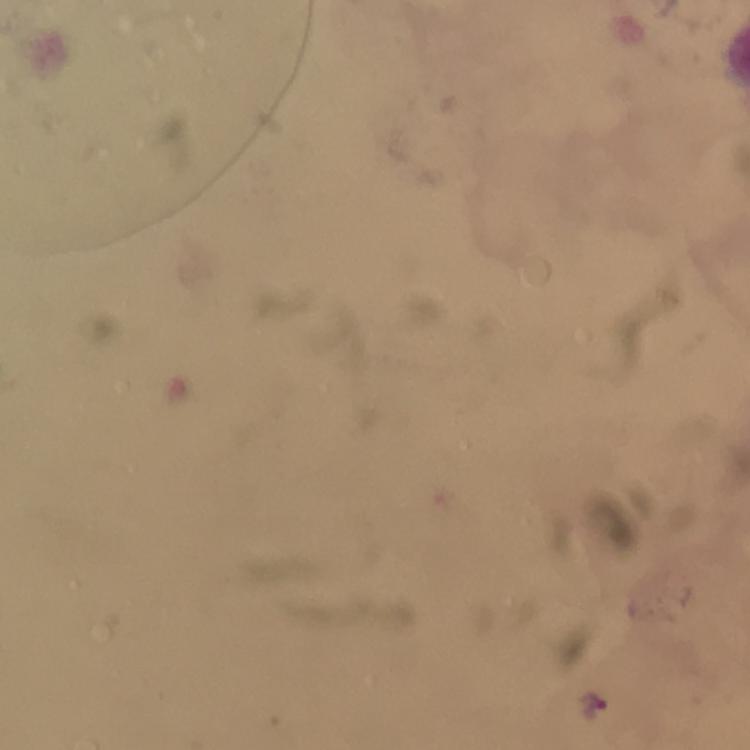

magnification: 100x
context: from a malaria diagnostic workup
immersion_oil: used
capture: smartphone mounted on the microscope
cropped_from: one field of view
plasmodium_parasite_locations: 'approximate centers as (x, y) in pixels: (592, 705)'
stain: Giemsa
image_size: 750×750 pixels
preparation: thick blood film